Outline each Plasmodium falciparum-infected red blood cell.
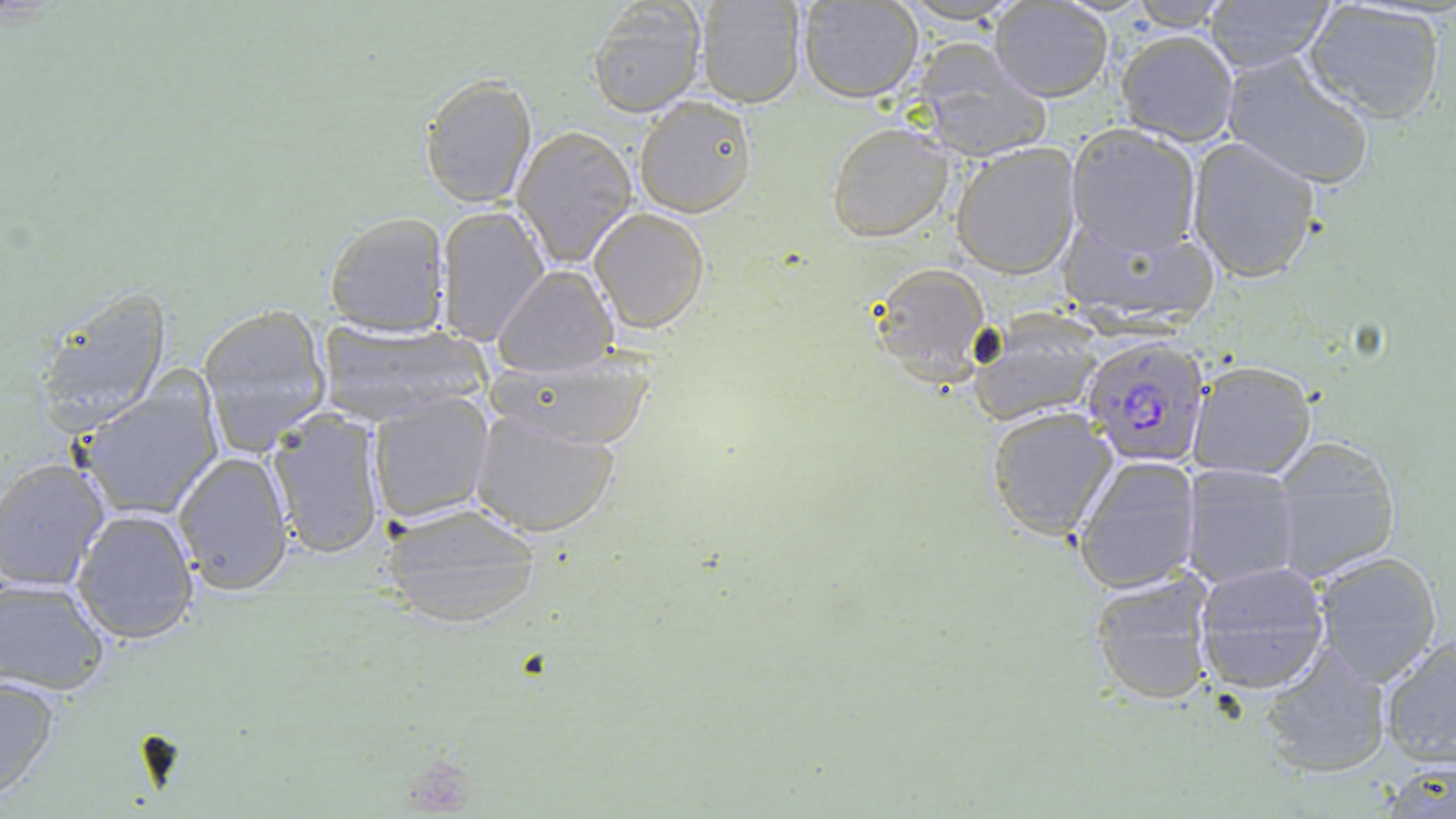

Approximate bounding boxes as (x1, y1, x2, y2) in pixels.
Plasmodium falciparum-infected red blood cells: (1082, 335, 1212, 467).

Uninfected red blood cell locations: (797, 0, 922, 102), (1121, 0, 1232, 31), (1198, 0, 1337, 73), (1302, 0, 1447, 125), (692, 1, 806, 107), (988, 1, 1114, 101), (585, 2, 705, 117), (1113, 30, 1240, 146), (914, 42, 1052, 161), (1221, 53, 1376, 191), (419, 73, 539, 209), (632, 93, 759, 218), (826, 122, 953, 242), (1064, 122, 1203, 259), (511, 126, 639, 267), (1184, 137, 1323, 283), (952, 143, 1082, 279), (436, 207, 549, 346), (590, 207, 709, 332), (325, 213, 450, 338), (1056, 214, 1219, 331), (868, 263, 992, 386), (493, 266, 618, 378), (30, 287, 171, 435), (195, 303, 334, 451), (970, 309, 1110, 425), (315, 318, 487, 425), (487, 345, 661, 451), (1187, 360, 1316, 480), (77, 381, 221, 519), (367, 391, 494, 526), (469, 404, 622, 537), (985, 407, 1118, 540), (267, 411, 387, 560), (1270, 436, 1400, 584), (173, 451, 295, 592), (1072, 455, 1201, 593), (0, 457, 110, 592), (1181, 463, 1302, 592), (379, 502, 542, 631), (72, 508, 201, 647), (1311, 550, 1444, 686), (1193, 560, 1331, 693), (1088, 568, 1216, 707), (0, 577, 112, 695), (1378, 633, 1456, 770), (1256, 643, 1394, 780), (0, 675, 59, 800). Slide-level diagnosis: Plasmodium falciparum. 1000x magnification. Optical microscopy. One field of a larger specimen. Thin blood film. Image is 1456×819 pixels. May-Grünwald-Giemsa-stained preparation.